Point out each Plasmodium parasite and each leukocyte.
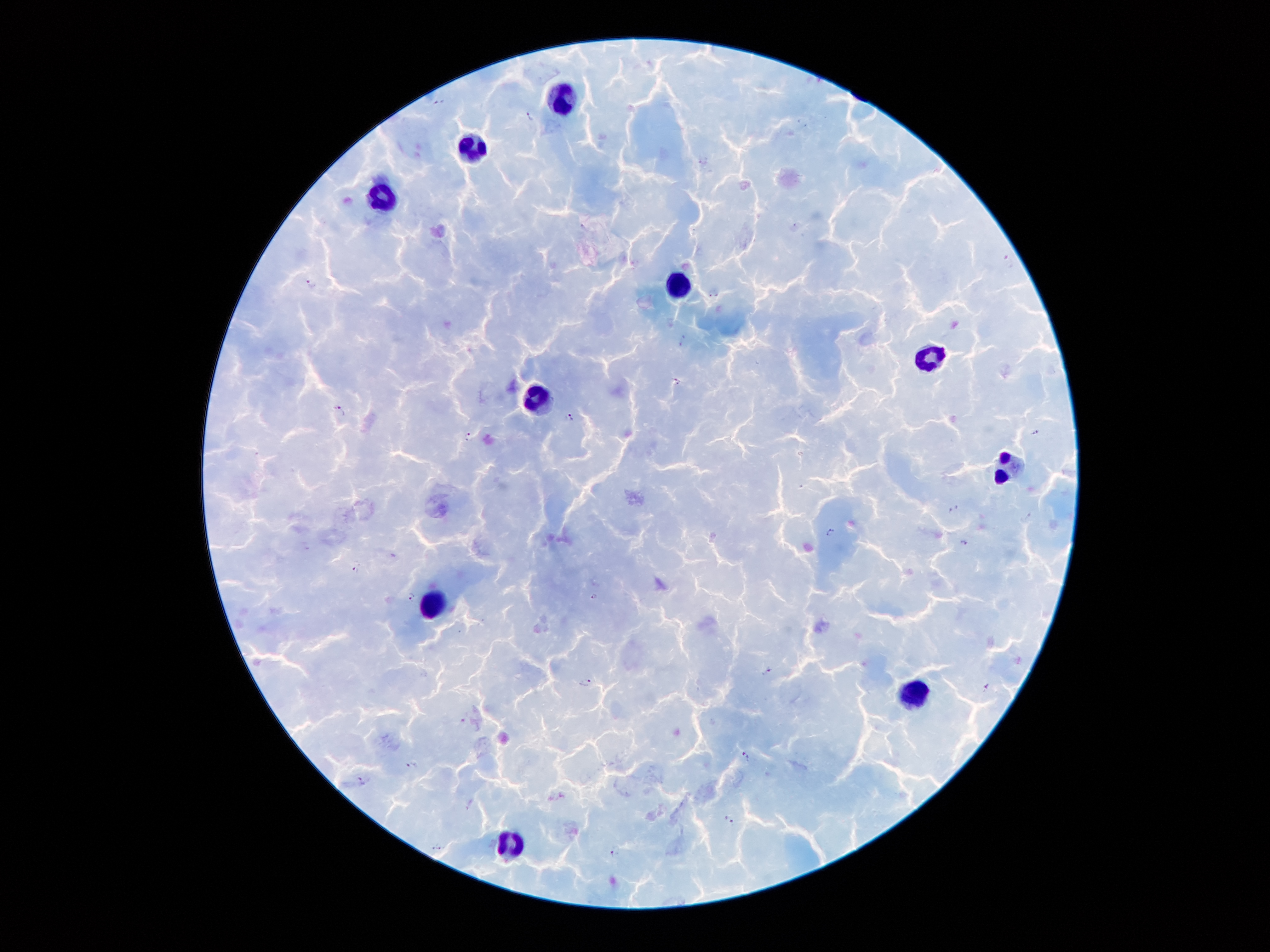

Approximate centers as {x, y} in pixels.
Plasmodium parasites: {441, 101}, {530, 115}, {705, 160}, {1008, 261}, {311, 283}, {677, 381}, {340, 410}, {569, 417}, {1037, 433}, {468, 438}, {953, 508}, {1028, 516}, {831, 531}, {965, 541}, {356, 569}, {411, 595}, {594, 595}, {767, 670}, {585, 681}, {986, 686}, {746, 756}, {412, 766}, {360, 781}, {469, 802}, {729, 819}, {437, 844}, {616, 851}.
Leukocytes: {564, 98}, {473, 146}, {379, 197}, {678, 283}, {931, 359}, {536, 399}, {1009, 466}, {432, 607}, {914, 692}, {510, 842}.

Image is 1270×952 pixels. Giemsa stain. Smartphone photograph taken through the microscope eyepiece. Thick peripheral-blood smear. One field from this slide. 100x magnification. Patient malaria status: infected with Plasmodium falciparum.